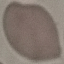

Summary:
  - Result: negative for malaria parasites
  - Capture: smartphone camera at the microscope eyepiece
  - Image type: cell patch, automatically extracted from a larger field of view and resized to 64 × 64 pixels
  - Preparation: thin blood smear
  - Stain: Giemsa